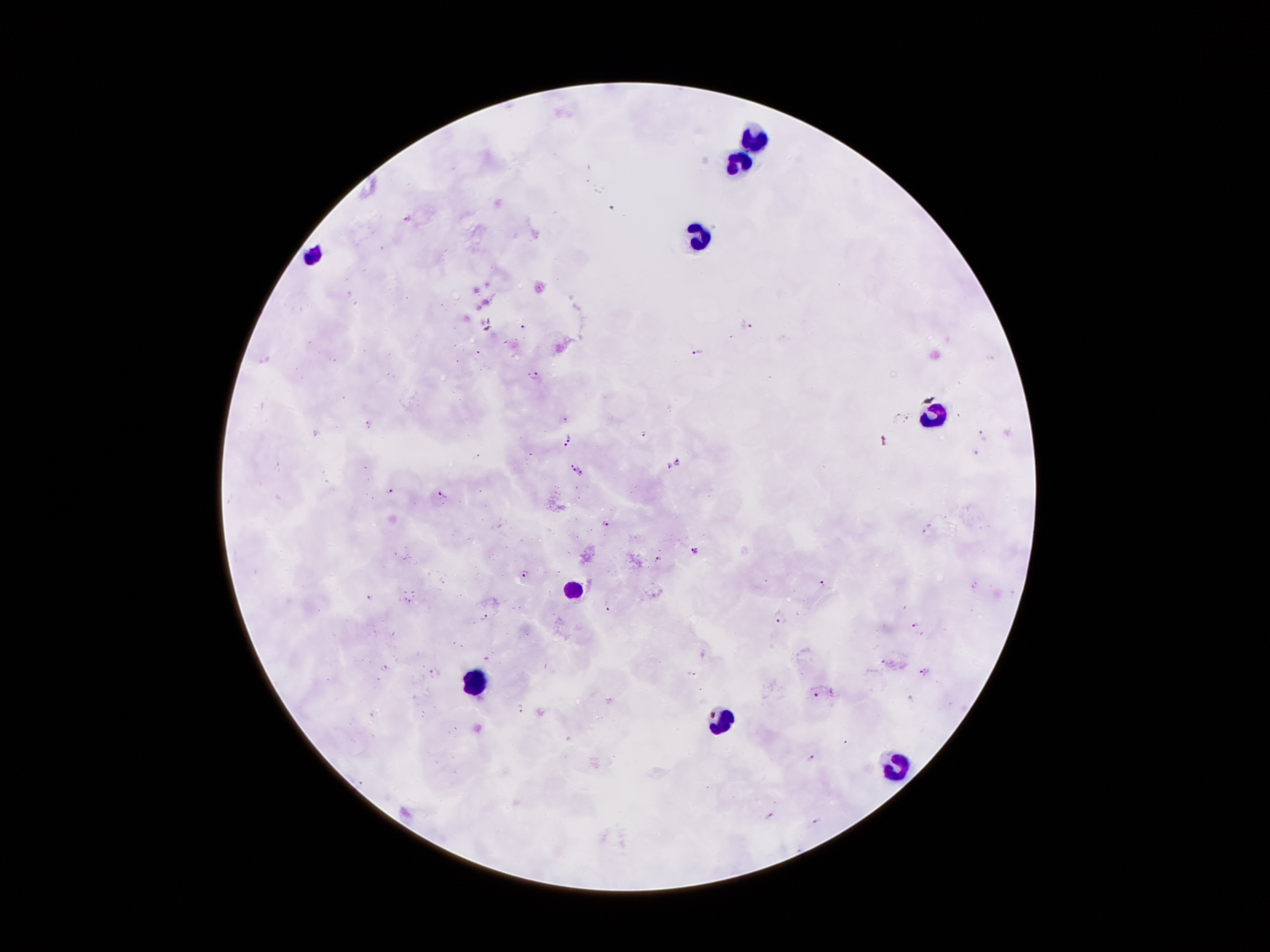
Approximate centers as {x, y} in pixels. Plasmodium parasite locations: {408, 218}, {524, 326}, {750, 326}, {696, 354}, {536, 375}, {567, 418}, {369, 425}, {986, 434}, {644, 435}, {572, 437}, {563, 448}, {976, 454}, {677, 463}, {573, 465}, {666, 466}, {581, 473}, {391, 490}, {443, 494}, {606, 523}, {696, 550}, {660, 558}, {526, 573}, {823, 584}, {370, 599}, {608, 608}, {484, 616}, {780, 619}, {915, 625}, {488, 658}, {883, 660}, {385, 669}, {435, 671}, {924, 672}, {690, 675}, {816, 696}, {520, 708}, {809, 758}, {771, 816}, {816, 821}. Leukocyte locations: {755, 142}, {740, 165}, {704, 231}, {314, 258}, {937, 413}, {576, 587}, {473, 681}, {725, 719}, {891, 765}. Patient malaria status: infected with Plasmodium falciparum. Giemsa stain. Image is 1270×952 pixels. Thick blood smear. Smartphone photograph taken through the microscope eyepiece. One field from this slide. 100x magnification.